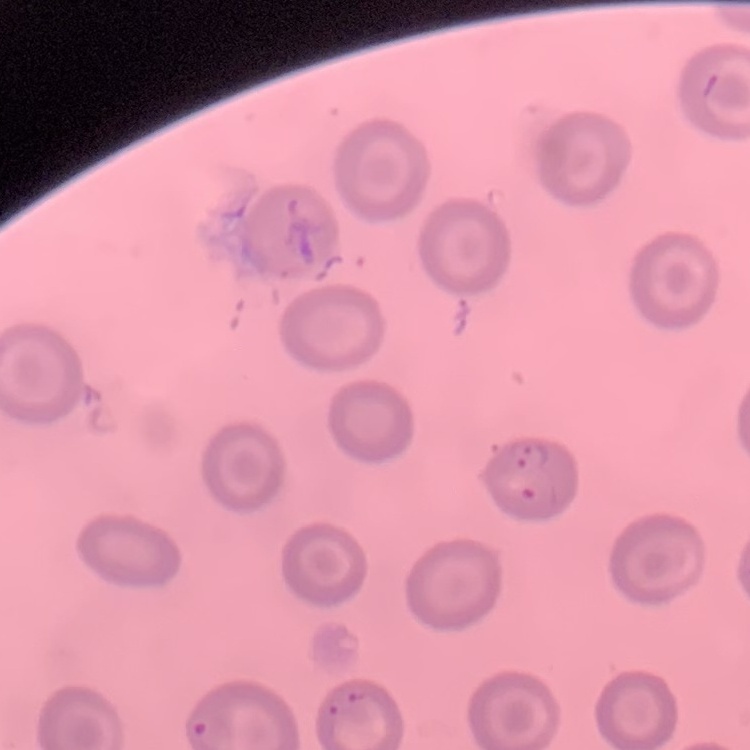
red_blood_cell_morphology: no rouleaux formation
stain: Field's or Giemsa
image_type: one tile cut from a larger photomicrograph
preparation: thin blood film